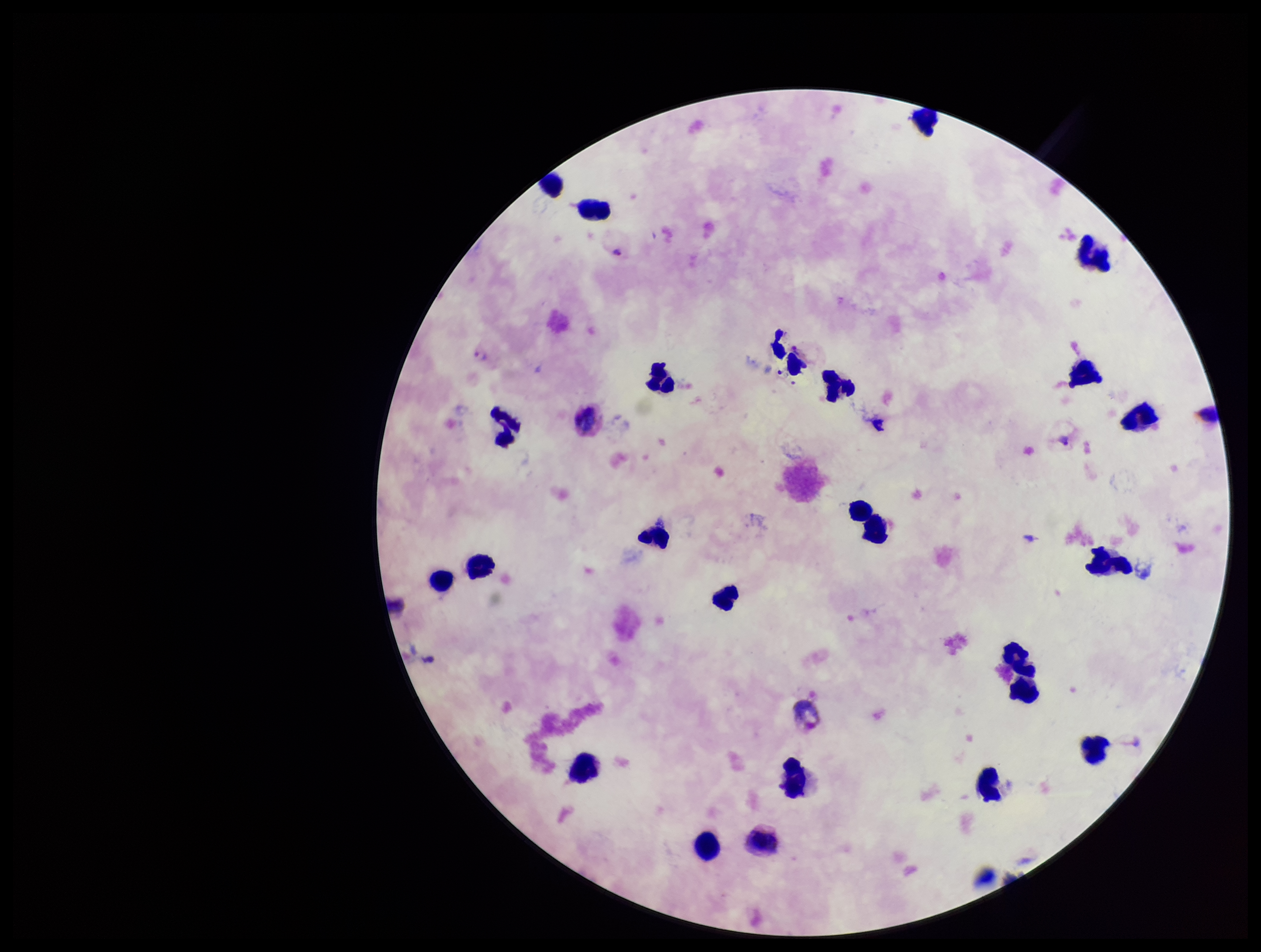

stain = Giemsa
parasite count = 2
preparation = thick blood smear
Plasmodium parasites = detected
field of view = single
species reported for this patient = Plasmodium vivax
leukocyte count = 22
capture = smartphone photograph through the microscope eyepiece
image size = 1261×952 pixels
patient malaria status = infected